Assess the morphology of the red blood cells.
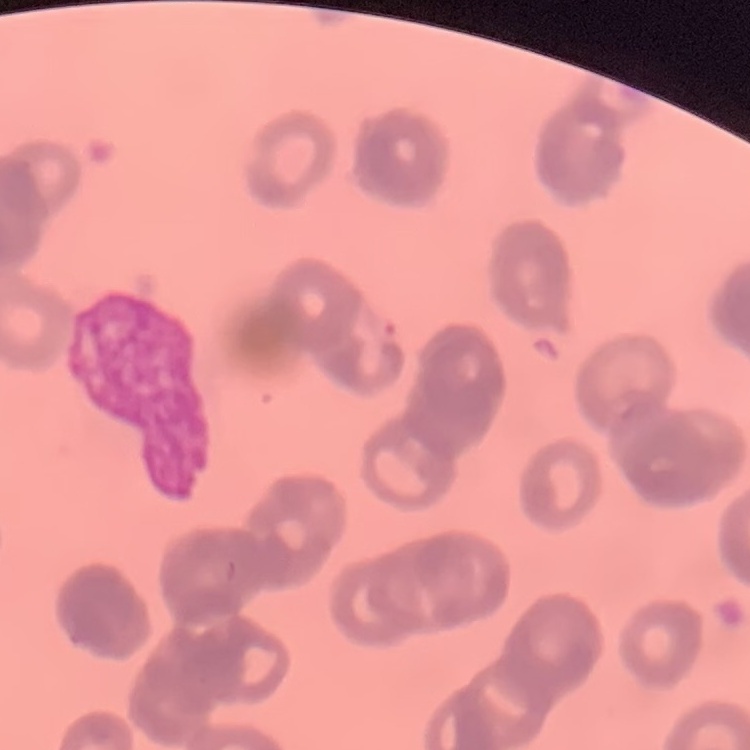

Rouleaux formation.

Summary:
  - Stain: Field's or Giemsa
  - Image type: one tile cut from a larger photomicrograph
  - Preparation: thin blood smear